Report the malaria status of this cell.
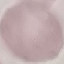
Uninfected.

Photographed with a smartphone camera at the microscope eyepiece. Giemsa-stained preparation. Thin blood film. Cell patch, automatically extracted from a larger field of view and resized to 64 × 64 pixels.